Identify the blood parasite species.
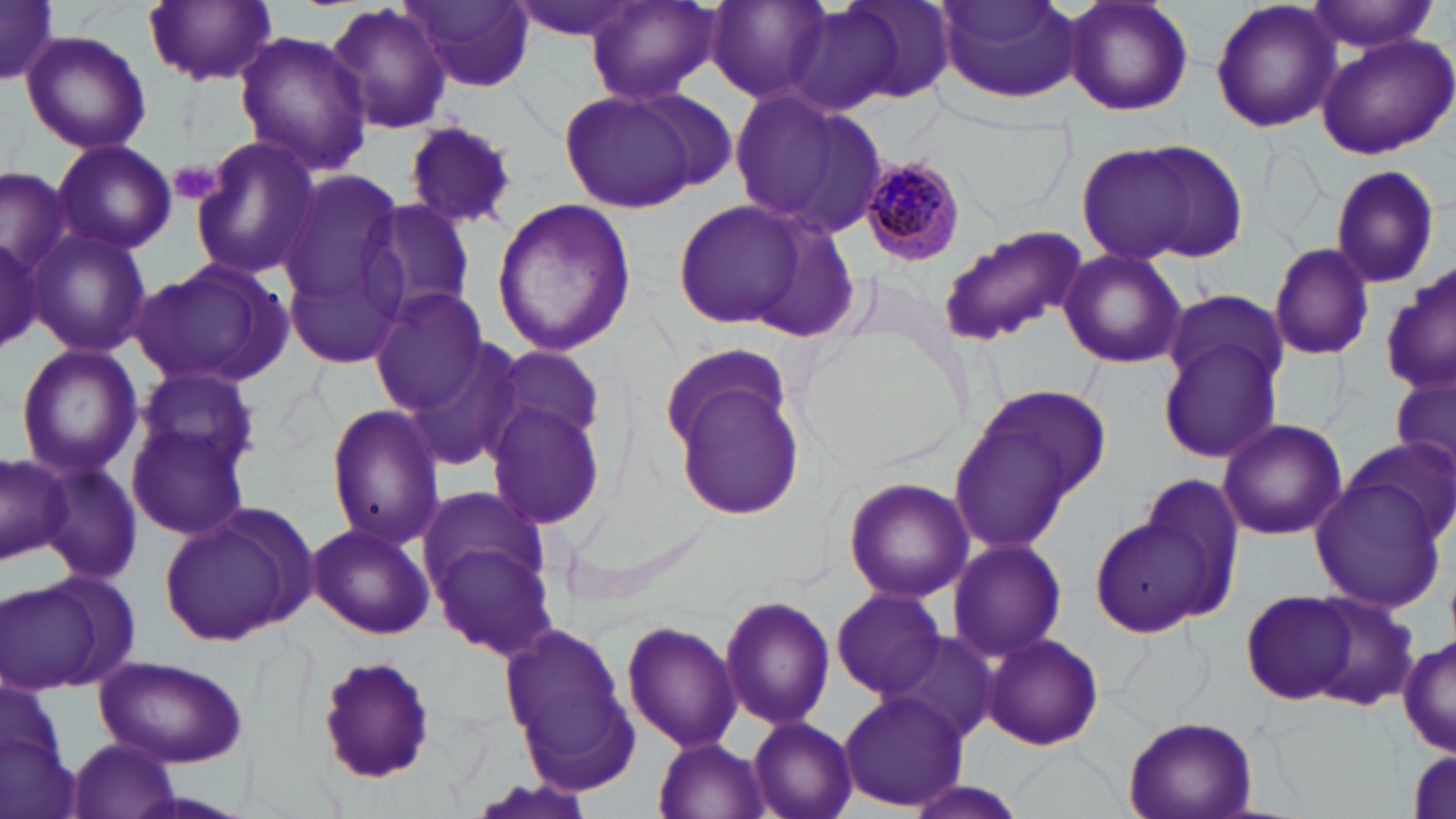

Plasmodium malariae.

Approximate bounding boxes as (x1, y1, x2, y2) in pixels. Platelet locations: (171, 159, 223, 205). Uninfected red blood cell locations: (402, 0, 538, 94), (504, 0, 649, 41), (702, 0, 840, 105), (799, 0, 957, 109), (934, 0, 1082, 104), (1061, 0, 1194, 115), (1209, 0, 1344, 135), (0, 1, 60, 86), (143, 1, 278, 87), (326, 1, 454, 138), (583, 1, 722, 107), (1304, 1, 1437, 55), (19, 30, 151, 154), (233, 31, 373, 178), (1315, 33, 1456, 158), (728, 87, 889, 236), (561, 88, 703, 212), (402, 116, 521, 232), (188, 135, 322, 282), (1075, 137, 1247, 267), (50, 139, 177, 256), (1329, 164, 1443, 289), (1, 166, 75, 275), (275, 174, 415, 367), (670, 196, 827, 334), (491, 197, 636, 356), (359, 200, 476, 322), (937, 225, 1086, 345), (0, 226, 50, 356), (29, 227, 151, 360), (1268, 241, 1375, 359), (1058, 249, 1187, 369), (130, 254, 296, 390), (1378, 268, 1456, 392), (368, 288, 491, 412), (1163, 291, 1289, 402), (397, 331, 529, 474), (1160, 336, 1287, 462), (479, 340, 608, 459), (657, 340, 794, 457), (14, 344, 144, 477), (1391, 368, 1456, 481), (133, 369, 258, 476), (669, 374, 807, 524), (948, 380, 1114, 553), (480, 384, 610, 531), (325, 404, 444, 548), (1216, 418, 1349, 539), (127, 419, 252, 541), (1347, 434, 1453, 543), (0, 451, 71, 565), (39, 458, 143, 586), (1133, 475, 1249, 619), (1309, 475, 1449, 611), (844, 477, 973, 603), (415, 483, 547, 610), (158, 502, 318, 648), (1088, 514, 1221, 641), (424, 518, 561, 664), (305, 521, 437, 640), (946, 539, 1067, 664), (2, 575, 119, 691), (830, 586, 950, 700), (1241, 590, 1356, 705), (1301, 593, 1420, 709), (717, 595, 835, 730), (498, 618, 638, 790), (621, 620, 739, 754), (879, 631, 998, 747), (981, 633, 1105, 750), (1398, 635, 1455, 757), (91, 653, 247, 767), (314, 656, 440, 786), (0, 678, 79, 819), (839, 687, 966, 811), (1123, 713, 1260, 819), (748, 717, 858, 819), (653, 736, 772, 819), (63, 737, 185, 819), (1408, 749, 1453, 817), (896, 777, 1032, 819). Plasmodium malariae-infected red blood cell locations: (854, 154, 967, 268). Image is 1456×819 pixels. Light microscopy. May-Grünwald-Giemsa-stained preparation. 1000x magnification. Thin blood film. One field of a larger specimen.